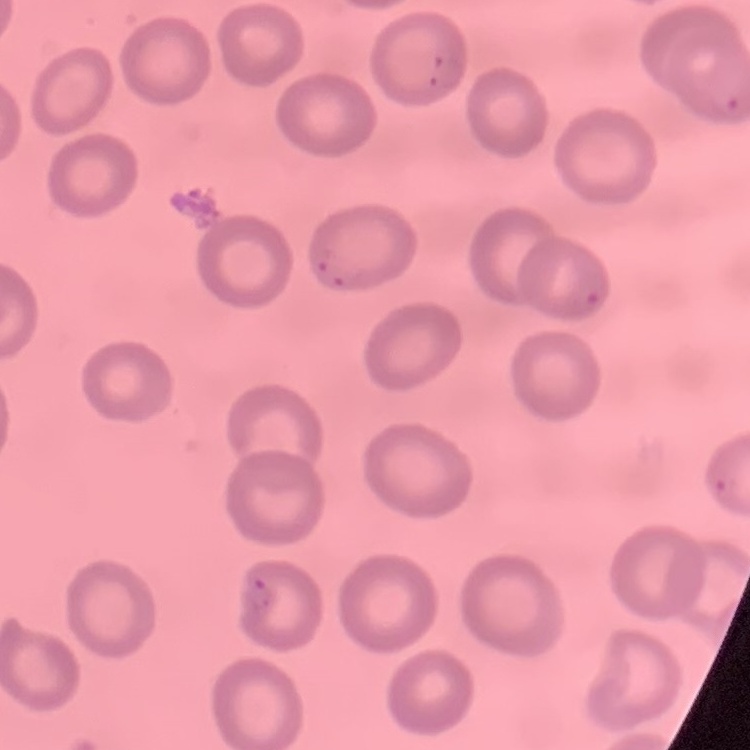 The erythrocytes exhibit no rouleaux formation. Square crop of a larger photomicrograph. Thin blood film. Stained with either Field's or Giemsa.